Outline each Plasmodium ovale-infected red blood cell.
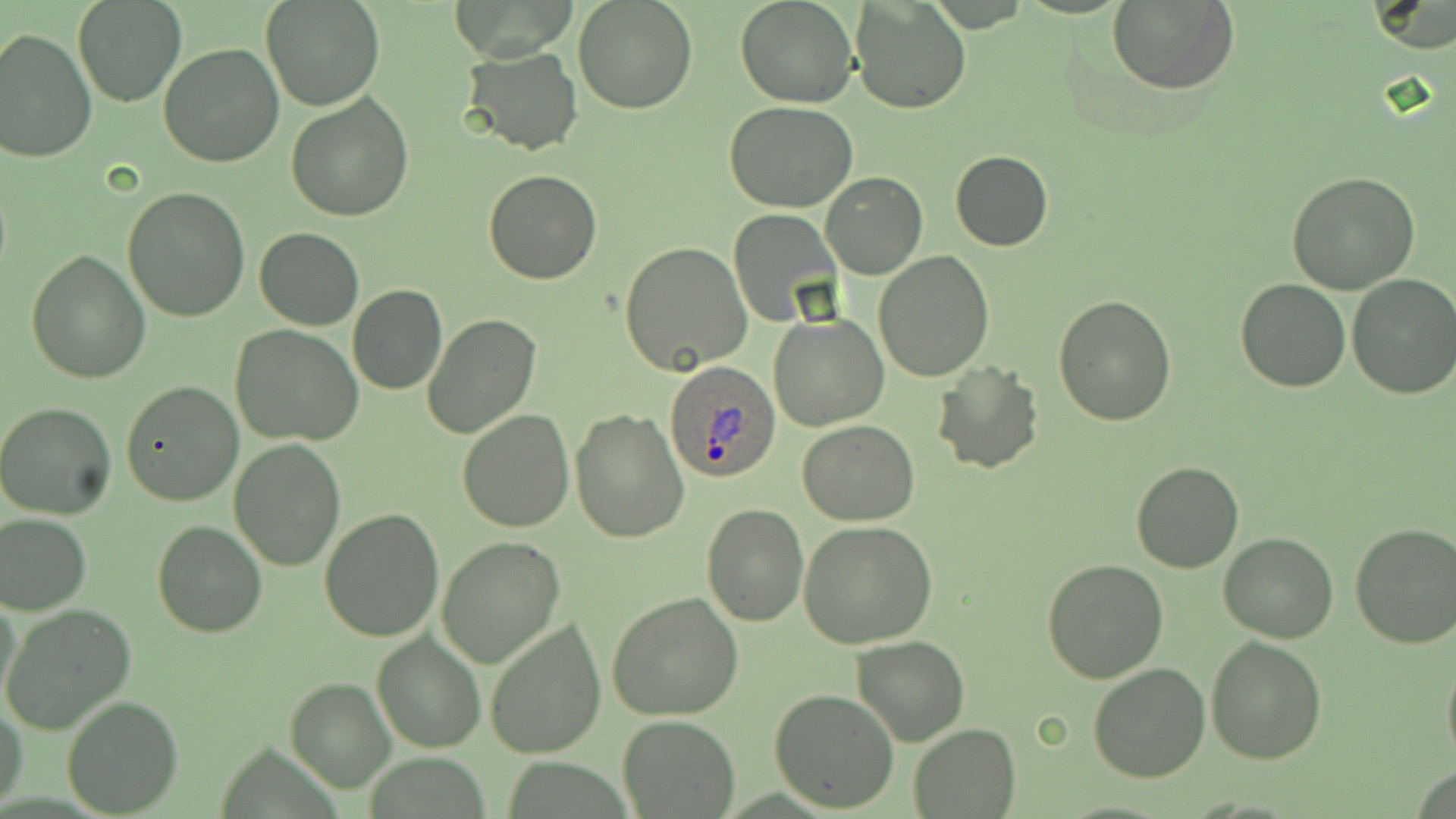
Approximate bounding boxes as named x1/y1/x2/y2 corners in pixels.
Plasmodium ovale-infected red blood cells: (x1=663, y1=361, x2=781, y2=483).

Uninfected red blood cell locations: (x1=73, y1=0, x2=188, y2=107), (x1=261, y1=0, x2=384, y2=111), (x1=572, y1=0, x2=699, y2=114), (x1=735, y1=0, x2=858, y2=107), (x1=1108, y1=0, x2=1240, y2=96), (x1=852, y1=2, x2=969, y2=114), (x1=0, y1=28, x2=96, y2=162), (x1=158, y1=42, x2=286, y2=168), (x1=460, y1=45, x2=583, y2=155), (x1=285, y1=93, x2=414, y2=223), (x1=724, y1=102, x2=857, y2=213), (x1=949, y1=150, x2=1054, y2=251), (x1=482, y1=170, x2=602, y2=285), (x1=821, y1=171, x2=928, y2=278), (x1=1286, y1=172, x2=1423, y2=295), (x1=122, y1=188, x2=252, y2=322), (x1=727, y1=210, x2=839, y2=326), (x1=255, y1=227, x2=364, y2=330), (x1=619, y1=242, x2=753, y2=377), (x1=27, y1=250, x2=150, y2=384), (x1=873, y1=251, x2=994, y2=381), (x1=1347, y1=274, x2=1456, y2=399), (x1=1234, y1=279, x2=1350, y2=392), (x1=348, y1=285, x2=446, y2=396), (x1=1053, y1=294, x2=1179, y2=426), (x1=423, y1=314, x2=542, y2=440), (x1=769, y1=314, x2=888, y2=430), (x1=231, y1=325, x2=364, y2=446), (x1=932, y1=362, x2=1043, y2=475), (x1=122, y1=380, x2=244, y2=506), (x1=0, y1=400, x2=118, y2=520), (x1=571, y1=407, x2=688, y2=542), (x1=457, y1=410, x2=573, y2=533), (x1=797, y1=421, x2=920, y2=525), (x1=227, y1=438, x2=347, y2=572), (x1=1130, y1=461, x2=1244, y2=574), (x1=701, y1=503, x2=807, y2=625), (x1=319, y1=508, x2=444, y2=642), (x1=0, y1=512, x2=92, y2=616), (x1=152, y1=521, x2=268, y2=638), (x1=797, y1=522, x2=937, y2=648), (x1=1349, y1=523, x2=1456, y2=649), (x1=1218, y1=533, x2=1340, y2=642), (x1=436, y1=537, x2=564, y2=667), (x1=1042, y1=558, x2=1167, y2=682), (x1=609, y1=590, x2=745, y2=720), (x1=1, y1=591, x2=24, y2=708), (x1=2, y1=605, x2=136, y2=734), (x1=483, y1=617, x2=606, y2=760), (x1=371, y1=632, x2=485, y2=753), (x1=1206, y1=635, x2=1327, y2=765), (x1=852, y1=636, x2=969, y2=746), (x1=1441, y1=649, x2=1456, y2=768), (x1=1088, y1=662, x2=1212, y2=782), (x1=284, y1=675, x2=397, y2=793), (x1=767, y1=689, x2=899, y2=813), (x1=61, y1=695, x2=183, y2=815), (x1=1, y1=703, x2=26, y2=811), (x1=618, y1=714, x2=740, y2=819), (x1=908, y1=723, x2=1021, y2=818). Slide-level diagnosis: Plasmodium ovale. Single field of view. Optical microscopy. Thin blood film. 1000x magnification. May-Grünwald-Giemsa stain. Image is 1456×819 pixels.